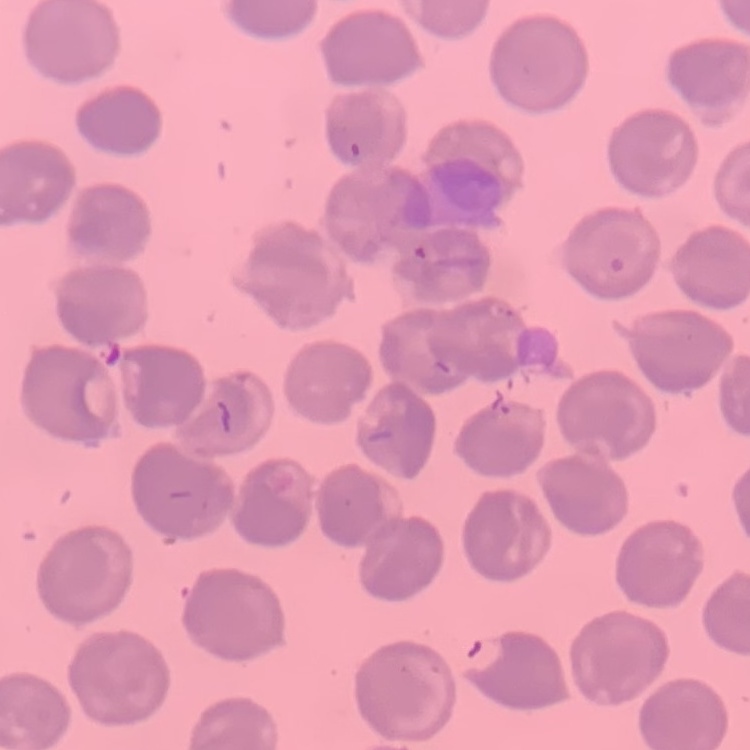

erythrocyte_morphology: no rouleaux formation
preparation: thin peripheral smear
stain: Field's or Giemsa
image_type: square crop of a larger photomicrograph